Name the blood parasite species.
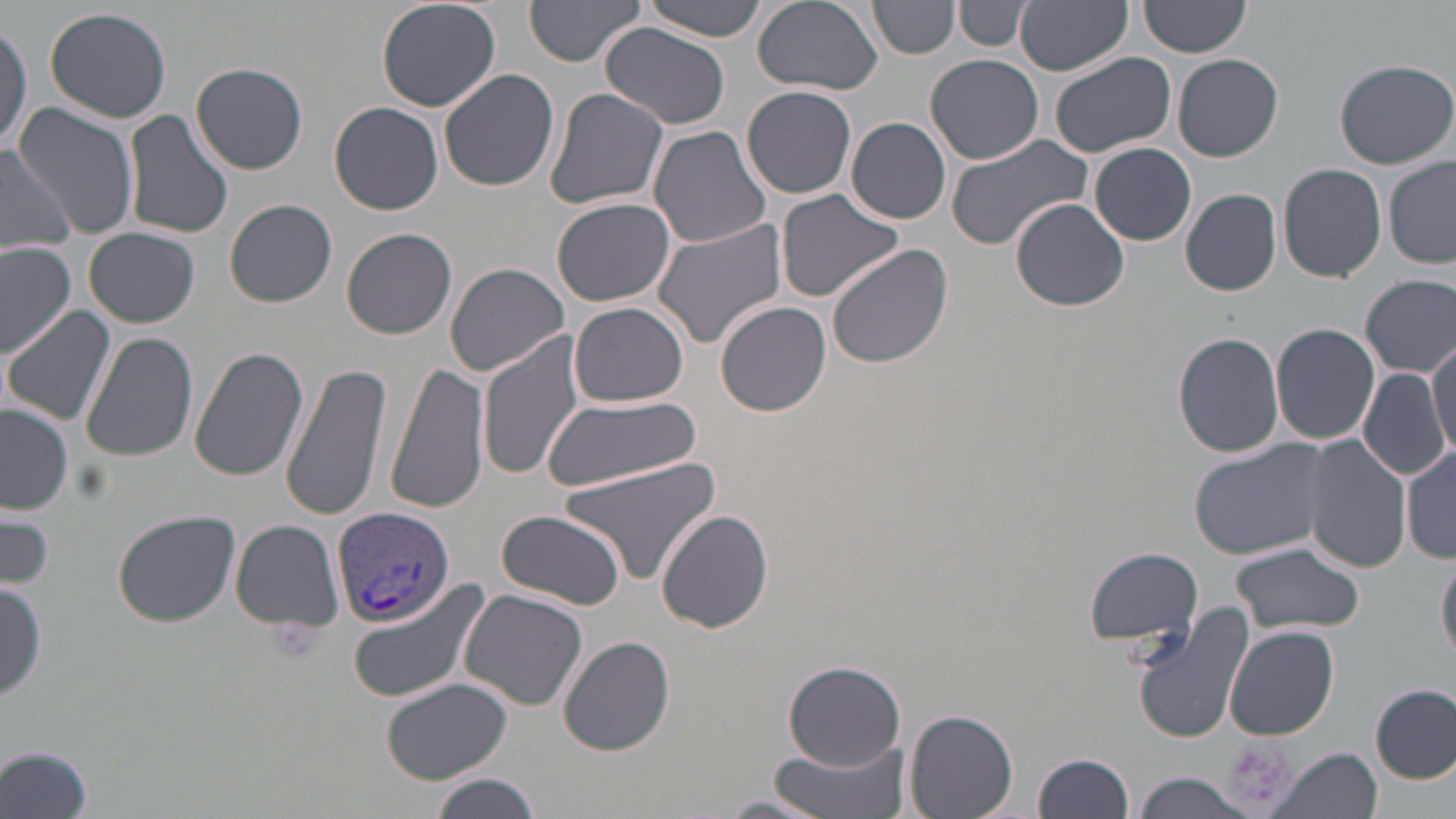
Plasmodium vivax.

uninfected red blood cell locations = approximate bounding boxes as (x1, y1, x2, y2) in pixels: (375, 0, 502, 112), (637, 0, 775, 41), (750, 0, 884, 94), (869, 0, 960, 58), (1016, 0, 1131, 75), (1140, 0, 1253, 57), (524, 2, 645, 68), (954, 2, 1033, 53), (44, 6, 173, 124), (0, 16, 31, 160), (600, 24, 731, 129), (1050, 52, 1175, 159), (925, 55, 1044, 165), (1173, 55, 1283, 162), (1333, 60, 1456, 168), (190, 62, 310, 175), (439, 68, 560, 192), (740, 86, 858, 199), (543, 87, 670, 211), (331, 102, 444, 215), (12, 103, 141, 239), (123, 107, 235, 241), (845, 116, 950, 224), (648, 124, 772, 247), (946, 133, 1095, 251), (0, 142, 79, 255), (1089, 142, 1196, 246), (1385, 158, 1456, 269), (1278, 162, 1388, 281), (1181, 188, 1282, 296), (774, 190, 906, 302), (553, 198, 675, 307), (1009, 198, 1130, 312), (225, 199, 337, 307), (652, 217, 791, 352), (85, 227, 200, 328), (343, 227, 457, 341), (0, 240, 75, 360), (827, 245, 954, 370), (444, 262, 569, 376), (1361, 274, 1456, 377), (570, 301, 690, 407), (717, 302, 832, 417), (4, 307, 117, 425), (1271, 322, 1380, 446), (79, 331, 199, 464), (1174, 331, 1285, 458), (479, 333, 586, 481), (1428, 334, 1455, 461), (187, 346, 310, 481), (281, 360, 393, 521), (386, 360, 490, 516), (1360, 366, 1448, 484), (543, 395, 700, 489), (1, 405, 73, 514), (1303, 436, 1413, 574), (1188, 438, 1334, 560), (1402, 446, 1455, 564), (556, 456, 723, 585), (0, 509, 55, 590), (112, 509, 242, 627), (497, 510, 627, 609), (657, 510, 773, 632), (230, 520, 345, 633), (1230, 543, 1365, 635), (1083, 546, 1204, 649), (1437, 553, 1456, 667), (344, 577, 491, 703), (0, 579, 46, 704), (458, 590, 587, 710), (1132, 606, 1255, 744), (1225, 625, 1339, 742), (558, 635, 676, 756), (782, 660, 908, 769), (381, 678, 511, 783), (1373, 684, 1455, 783), (905, 710, 1018, 819), (767, 742, 912, 819), (0, 744, 96, 819), (1267, 747, 1382, 819), (1034, 751, 1135, 819), (429, 773, 542, 818), (1127, 773, 1257, 819), (713, 794, 829, 819)
modality = optical microscopy
magnification = 1000x
stain = May-Grünwald-Giemsa
Plasmodium vivax-infected red blood cell locations = approximate bounding boxes as (x1, y1, x2, y2) in pixels: (332, 505, 456, 626)
preparation = thin blood smear
image size = 1456×819 pixels
field of view = one of a larger specimen
platelet locations = approximate bounding boxes as (x1, y1, x2, y2) in pixels: (1218, 737, 1298, 811)